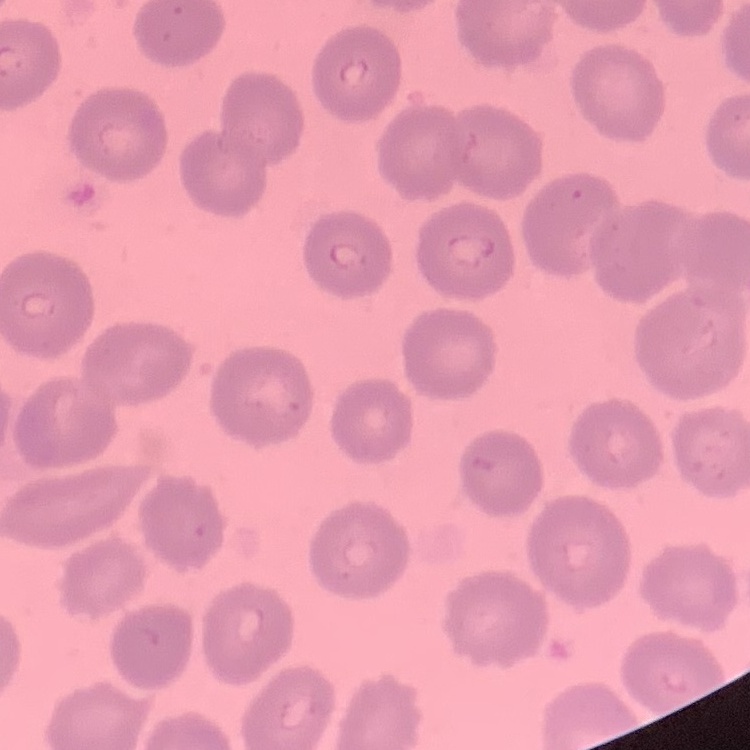
erythrocyte morphology = no rouleaux formation
preparation = thin blood smear
image type = one tile cut from a larger photomicrograph
stain = Field's or Giemsa